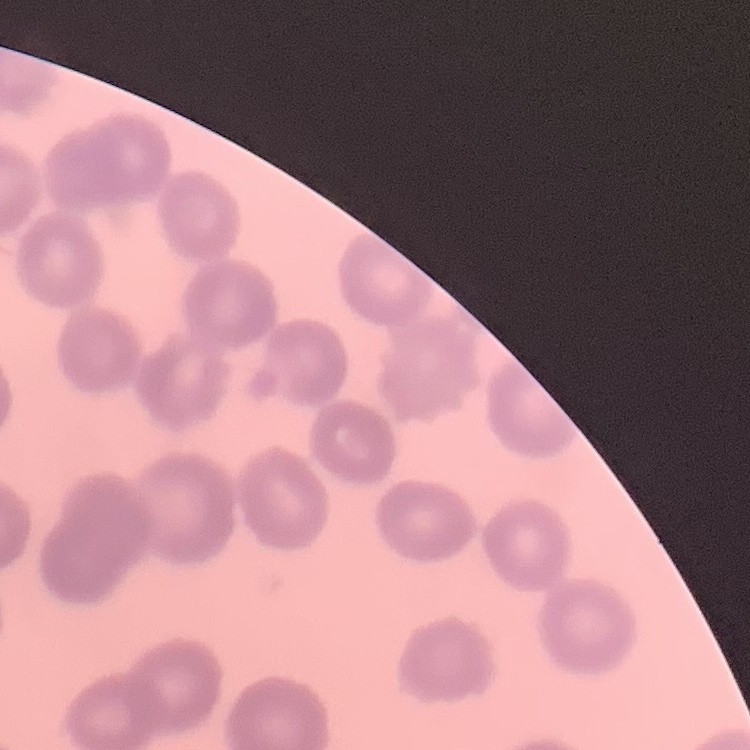

The erythrocytes show no rouleaux formation. One tile cut from a larger photomicrograph. Field's or Giemsa stain. Thin peripheral smear.